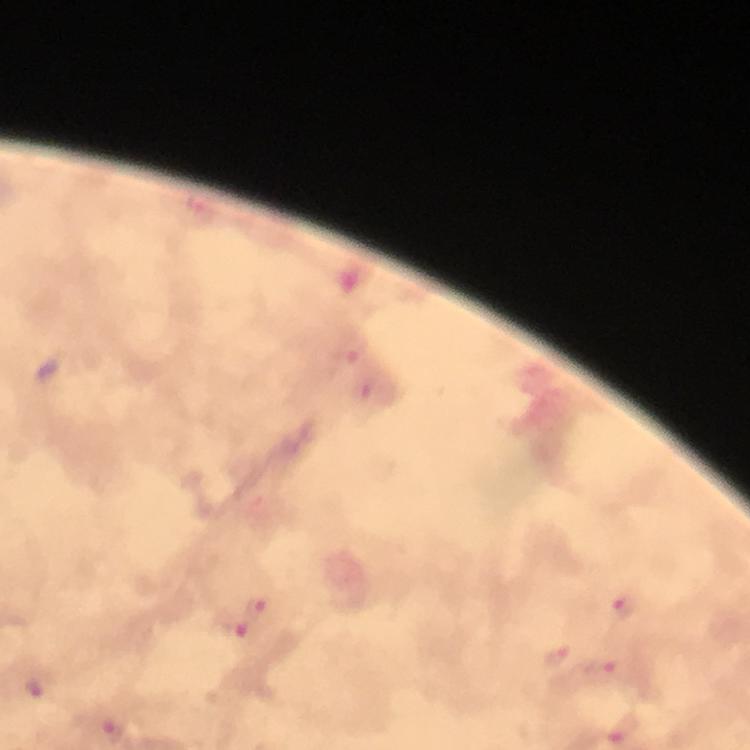

cropped from = a single field of view
magnification = 100x
immersion oil = used
capture = smartphone mounted on the microscope
preparation = thick smear
malaria parasite locations = approximate centers as [x, y] in pixels: [258, 607], [623, 608], [237, 627], [557, 659], [602, 669], [37, 687], [113, 729]
context = from a diagnostic examination for malaria
stain = Giemsa
image size = 750×750 pixels